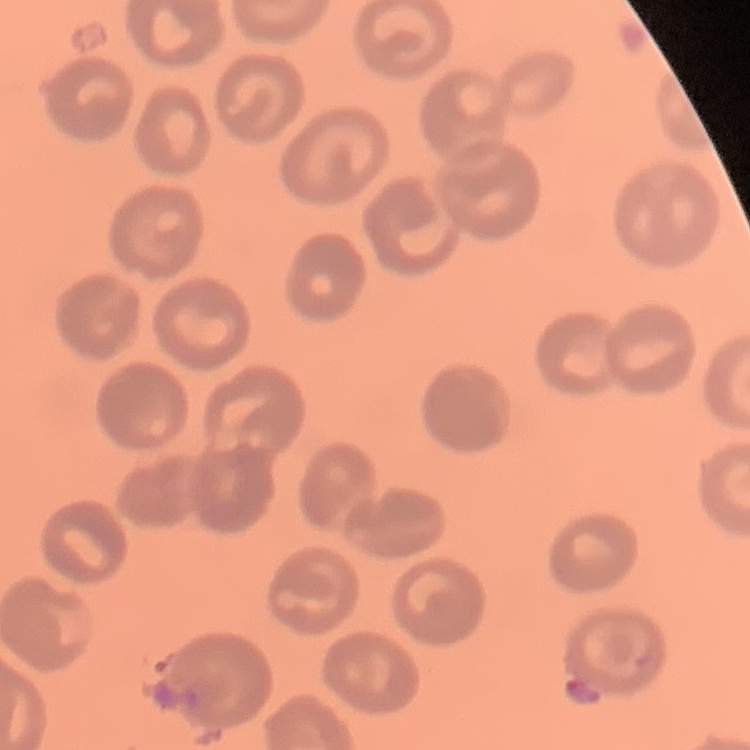

red_blood_cell_morphology: no rouleaux formation
image_type: one tile cut from a larger photomicrograph
preparation: thin peripheral smear
stain: Field's or Giemsa